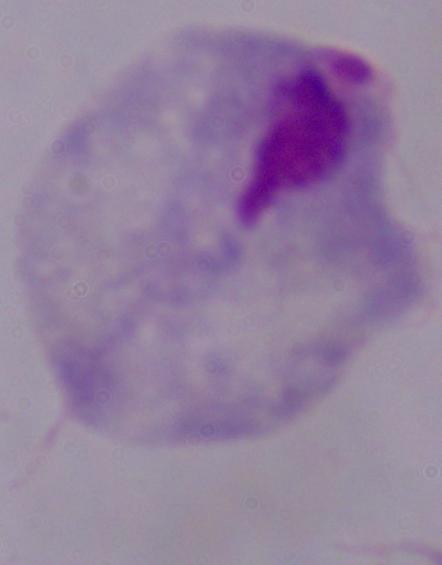

Summary:
  - Magnification: 1000x
  - Modality: micrograph
  - Identification: trichomonad